Report the malaria status of this cell.
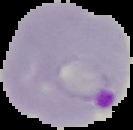

Parasitized.

image type = segmented cell region on a black background
image size = 133×130 pixels
preparation = thin blood film